State the blood parasite species.
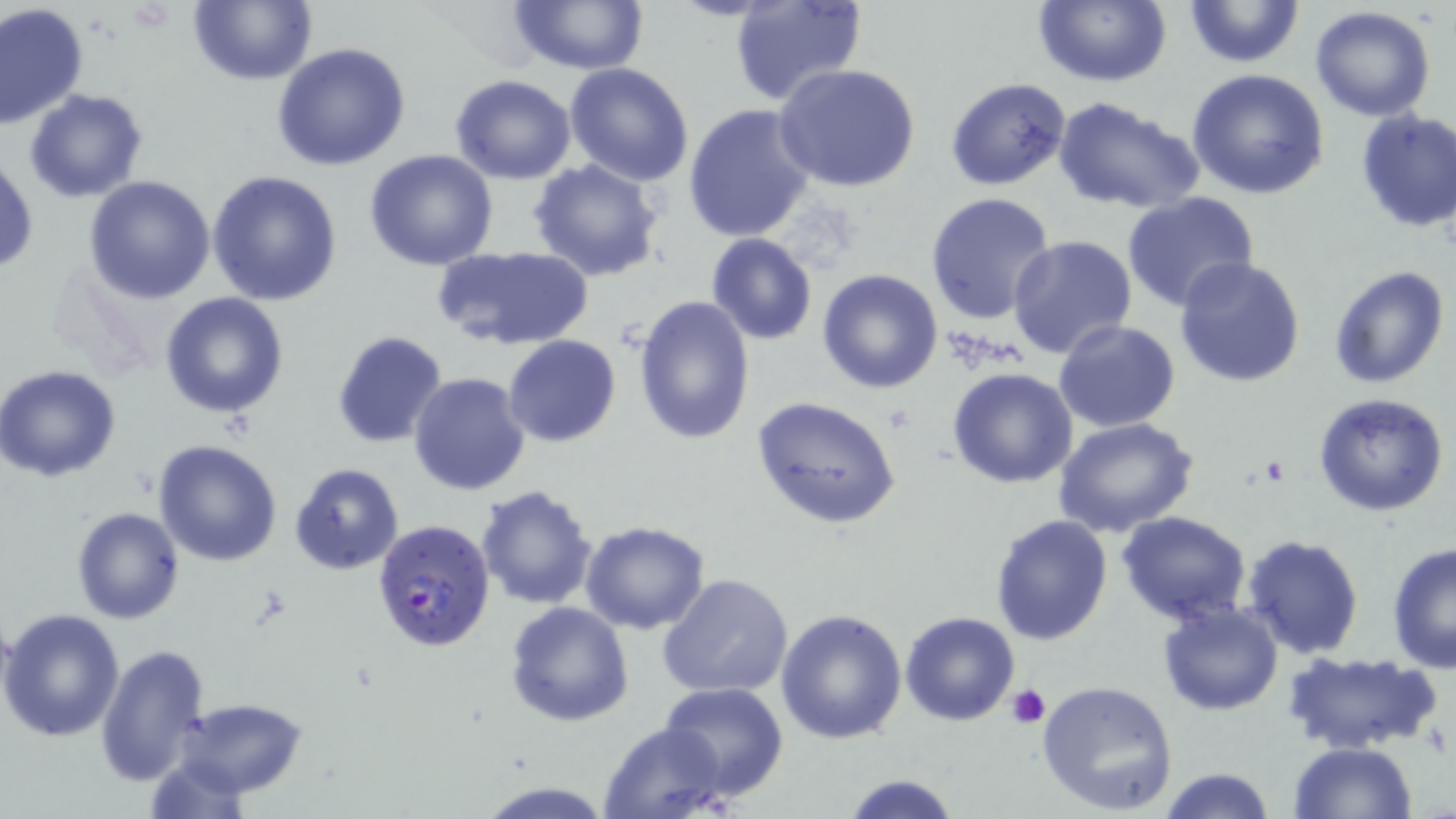

Plasmodium falciparum.

Approximate bounding boxes as (x1, y1, x2, y2) in pixels. Platelet locations: (1009, 685, 1052, 728). Uninfected red blood cell locations: (189, 0, 314, 86), (504, 0, 650, 74), (729, 0, 869, 109), (1032, 0, 1172, 88), (1183, 0, 1304, 69), (1, 5, 89, 131), (1308, 7, 1438, 122), (272, 43, 410, 172), (564, 63, 695, 186), (775, 63, 920, 193), (1187, 68, 1330, 199), (450, 74, 578, 184), (945, 77, 1071, 190), (24, 88, 148, 203), (1052, 95, 1205, 215), (682, 104, 817, 242), (1354, 109, 1456, 233), (364, 149, 499, 271), (1, 154, 37, 275), (528, 160, 664, 282), (209, 169, 342, 305), (84, 175, 216, 303), (925, 191, 1057, 326), (1121, 191, 1260, 313), (1007, 232, 1138, 358), (705, 233, 818, 344), (433, 245, 594, 350), (1173, 254, 1306, 389), (1330, 266, 1449, 388), (816, 268, 943, 393), (159, 293, 289, 418), (634, 293, 756, 445), (1053, 320, 1180, 434), (332, 331, 449, 447), (503, 334, 621, 448), (0, 365, 122, 482), (947, 367, 1079, 489), (408, 372, 529, 496), (1313, 393, 1452, 517), (751, 396, 900, 529), (1053, 418, 1200, 538), (153, 440, 282, 567), (289, 463, 403, 574), (476, 485, 598, 610), (71, 507, 185, 624), (1118, 510, 1252, 626), (988, 514, 1113, 647), (579, 521, 710, 634), (1241, 534, 1365, 660), (1386, 540, 1456, 672), (658, 573, 792, 699), (1157, 599, 1286, 715), (504, 600, 634, 726), (776, 607, 908, 744), (1, 608, 127, 742), (900, 611, 1021, 727), (95, 641, 212, 785), (1280, 649, 1440, 755), (1035, 678, 1179, 817), (659, 683, 788, 800), (174, 698, 307, 798), (599, 720, 732, 819), (1287, 741, 1418, 818), (142, 755, 252, 818), (1158, 766, 1275, 819), (840, 772, 963, 819), (477, 778, 612, 817). Plasmodium falciparum-infected red blood cell locations: (370, 518, 496, 654). One field of a larger specimen. Captured at 1000x magnification. May-Grünwald-Giemsa stain. Thin blood smear. Optical microscopy. Image is 1456×819 pixels.